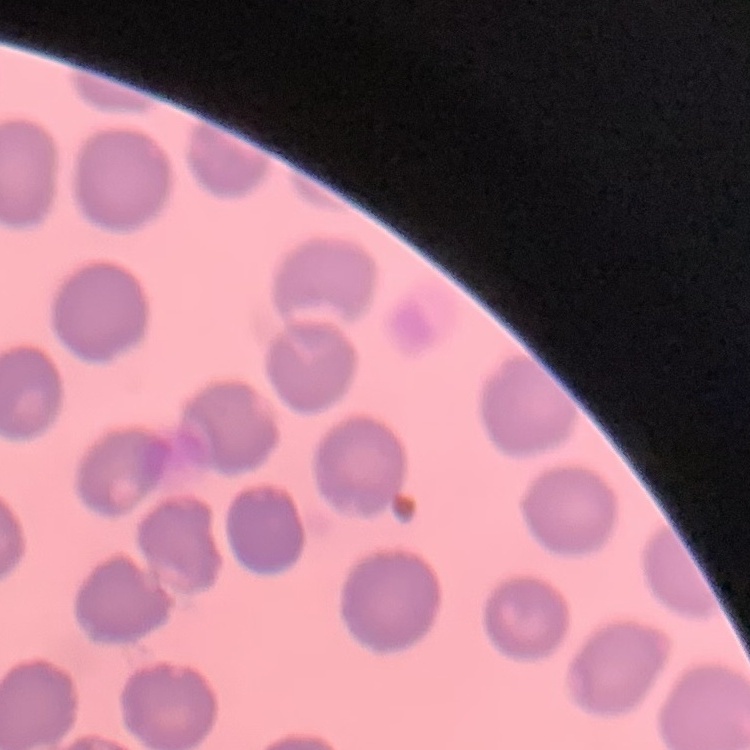
Summary:
  - Erythrocyte morphology: no rouleaux formation
  - Image type: one tile cut from a larger photomicrograph
  - Stain: Field's or Giemsa
  - Preparation: thin blood film